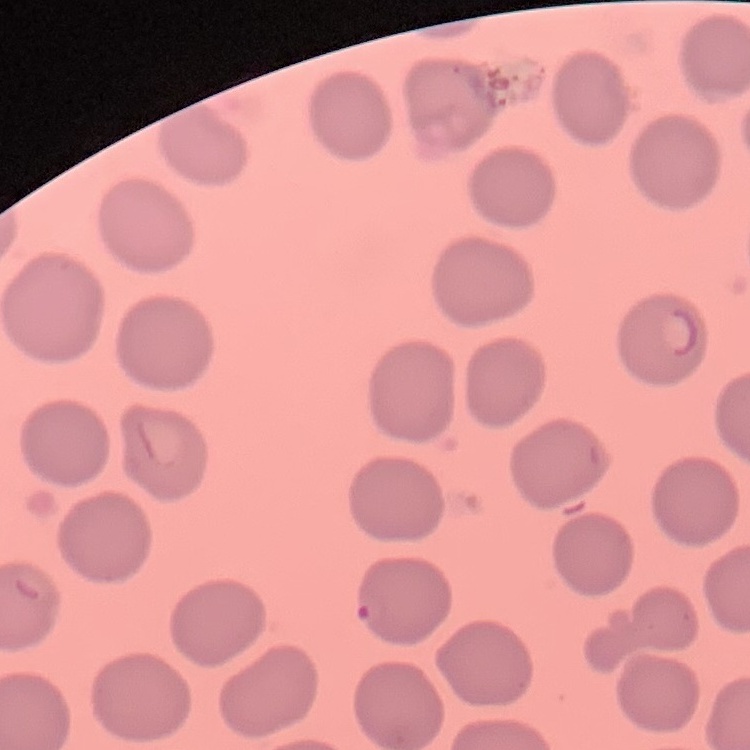

red blood cell morphology = no rouleaux formation
image type = square crop of a larger photomicrograph
stain = Field's or Giemsa
preparation = thin peripheral smear